Name the cell type shown.
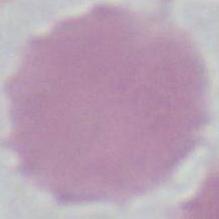

An erythrocyte.

1000x magnification. Photomicrograph.